Name the cell type shown.
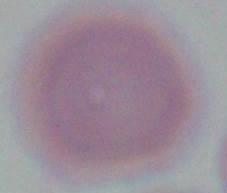
This is an erythrocyte.

1000x magnification. Micrograph.